State which parasite is depicted.
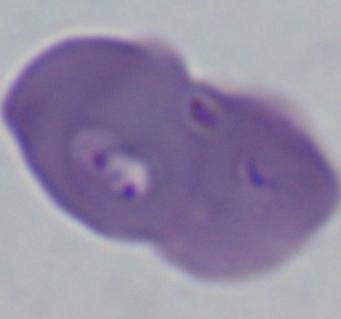
Babesia.

modality: micrograph
magnification: 1000x